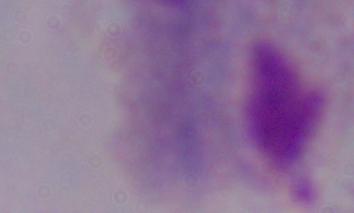
Summary:
  - Magnification: 1000x
  - Modality: photomicrograph
  - Identification: trichomonad